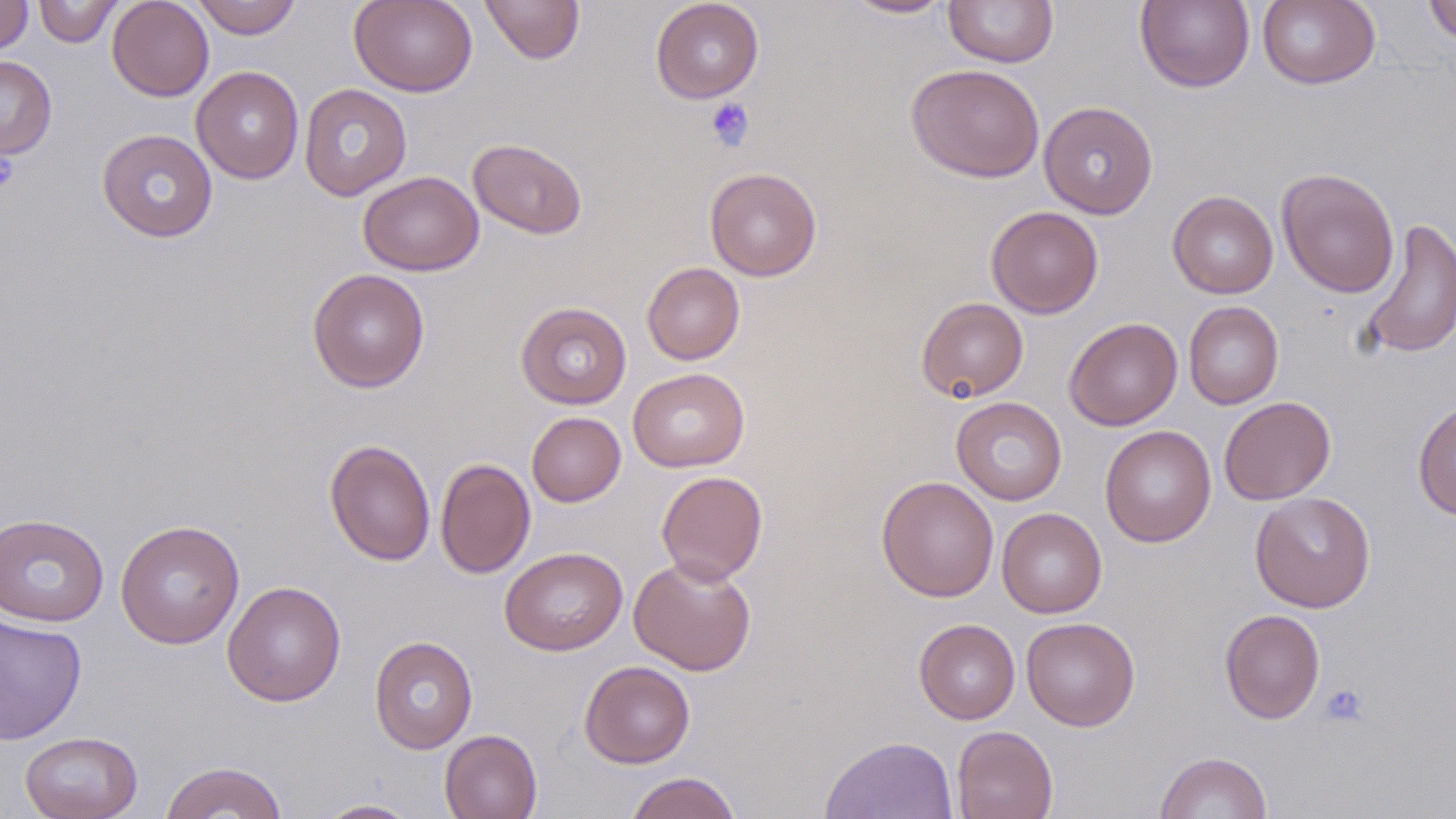
slide-level diagnosis = no evidence of blood parasites
stain = May-Grünwald-Giemsa
uninfected red blood cell locations = approximate bounding boxes as named x1/y1/x2/y2 corners in pixels: (x1=33, y1=0, x2=123, y2=47), (x1=107, y1=0, x2=214, y2=101), (x1=191, y1=0, x2=302, y2=39), (x1=349, y1=0, x2=478, y2=97), (x1=479, y1=0, x2=585, y2=65), (x1=650, y1=0, x2=764, y2=103), (x1=842, y1=0, x2=954, y2=19), (x1=943, y1=0, x2=1058, y2=67), (x1=1423, y1=0, x2=1456, y2=45), (x1=0, y1=1, x2=34, y2=54), (x1=1135, y1=1, x2=1255, y2=92), (x1=1257, y1=1, x2=1380, y2=90), (x1=0, y1=55, x2=57, y2=159), (x1=905, y1=64, x2=1045, y2=183), (x1=191, y1=66, x2=304, y2=184), (x1=299, y1=83, x2=412, y2=201), (x1=1039, y1=100, x2=1158, y2=219), (x1=96, y1=128, x2=218, y2=243), (x1=468, y1=138, x2=587, y2=240), (x1=704, y1=167, x2=822, y2=281), (x1=1277, y1=167, x2=1399, y2=298), (x1=359, y1=171, x2=483, y2=276), (x1=1167, y1=190, x2=1278, y2=299), (x1=986, y1=206, x2=1104, y2=318), (x1=1357, y1=216, x2=1455, y2=361), (x1=641, y1=262, x2=745, y2=365), (x1=307, y1=268, x2=430, y2=393), (x1=916, y1=296, x2=1029, y2=402), (x1=515, y1=301, x2=632, y2=409), (x1=1183, y1=301, x2=1284, y2=409), (x1=1064, y1=317, x2=1183, y2=431), (x1=628, y1=368, x2=749, y2=472), (x1=951, y1=396, x2=1067, y2=505), (x1=1219, y1=396, x2=1336, y2=505), (x1=1412, y1=400, x2=1456, y2=521), (x1=526, y1=411, x2=626, y2=507), (x1=1100, y1=425, x2=1216, y2=547), (x1=324, y1=439, x2=436, y2=566), (x1=435, y1=458, x2=536, y2=579), (x1=656, y1=470, x2=768, y2=584), (x1=876, y1=475, x2=998, y2=602), (x1=1249, y1=492, x2=1376, y2=613), (x1=996, y1=508, x2=1107, y2=618), (x1=0, y1=513, x2=109, y2=627), (x1=116, y1=519, x2=244, y2=649), (x1=500, y1=546, x2=628, y2=656), (x1=629, y1=556, x2=757, y2=675), (x1=222, y1=581, x2=346, y2=706), (x1=1220, y1=609, x2=1325, y2=724), (x1=0, y1=613, x2=88, y2=745), (x1=1022, y1=617, x2=1140, y2=731), (x1=913, y1=619, x2=1020, y2=724), (x1=369, y1=635, x2=478, y2=753), (x1=579, y1=660, x2=695, y2=768), (x1=951, y1=725, x2=1058, y2=819), (x1=440, y1=729, x2=542, y2=819), (x1=19, y1=731, x2=143, y2=819), (x1=821, y1=735, x2=958, y2=819), (x1=1155, y1=751, x2=1273, y2=819), (x1=158, y1=760, x2=289, y2=819), (x1=625, y1=771, x2=742, y2=819), (x1=313, y1=799, x2=423, y2=818)
image size = 1456×819 pixels
platelet locations = approximate bounding boxes as named x1/y1/x2/y2 corners in pixels: (x1=705, y1=97, x2=755, y2=151), (x1=0, y1=152, x2=19, y2=193), (x1=1320, y1=683, x2=1369, y2=726)
field of view = single
modality = optical microscopy
magnification = 1000x
preparation = thin blood smear